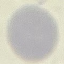

Result: no malaria parasites detected. Giemsa-stained preparation. Cell patch, automatically extracted from a larger field of view and resized to 64 × 64 pixels. Thin smear of blood. Acquired by smartphone through the microscope eyepiece.